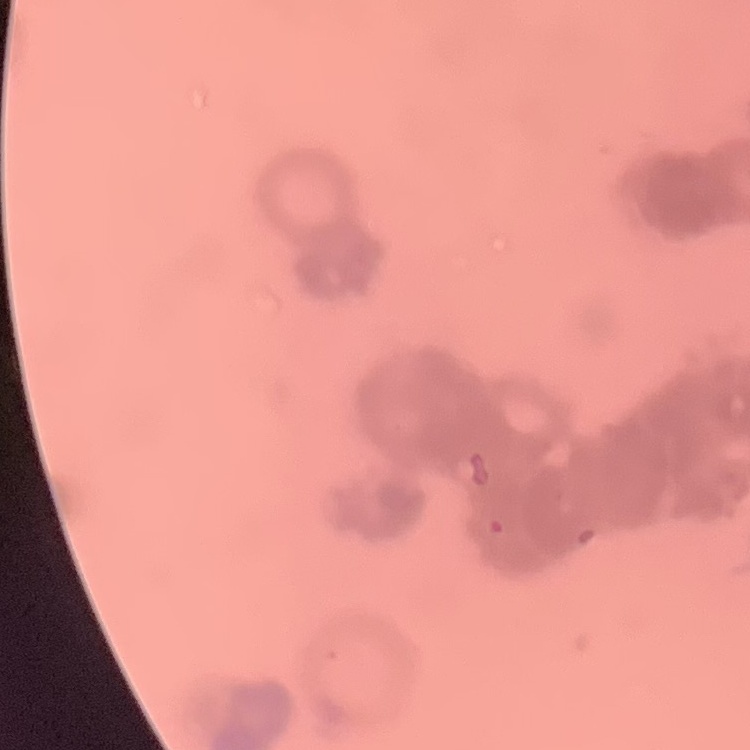 The red blood cells show rouleaux formation. Stained with either Field's or Giemsa. Thin blood film. Square crop of a larger photomicrograph.